Identify the parasite.
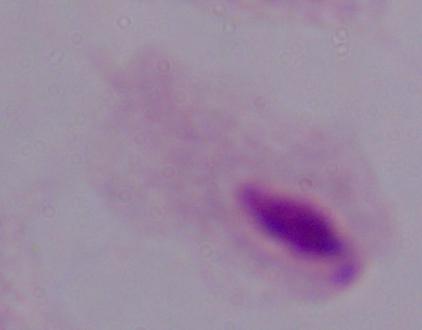
This is a trichomonad.

Summary:
  - Magnification: 1000x
  - Modality: micrograph